Give the extent of all uninfected red blood cells.
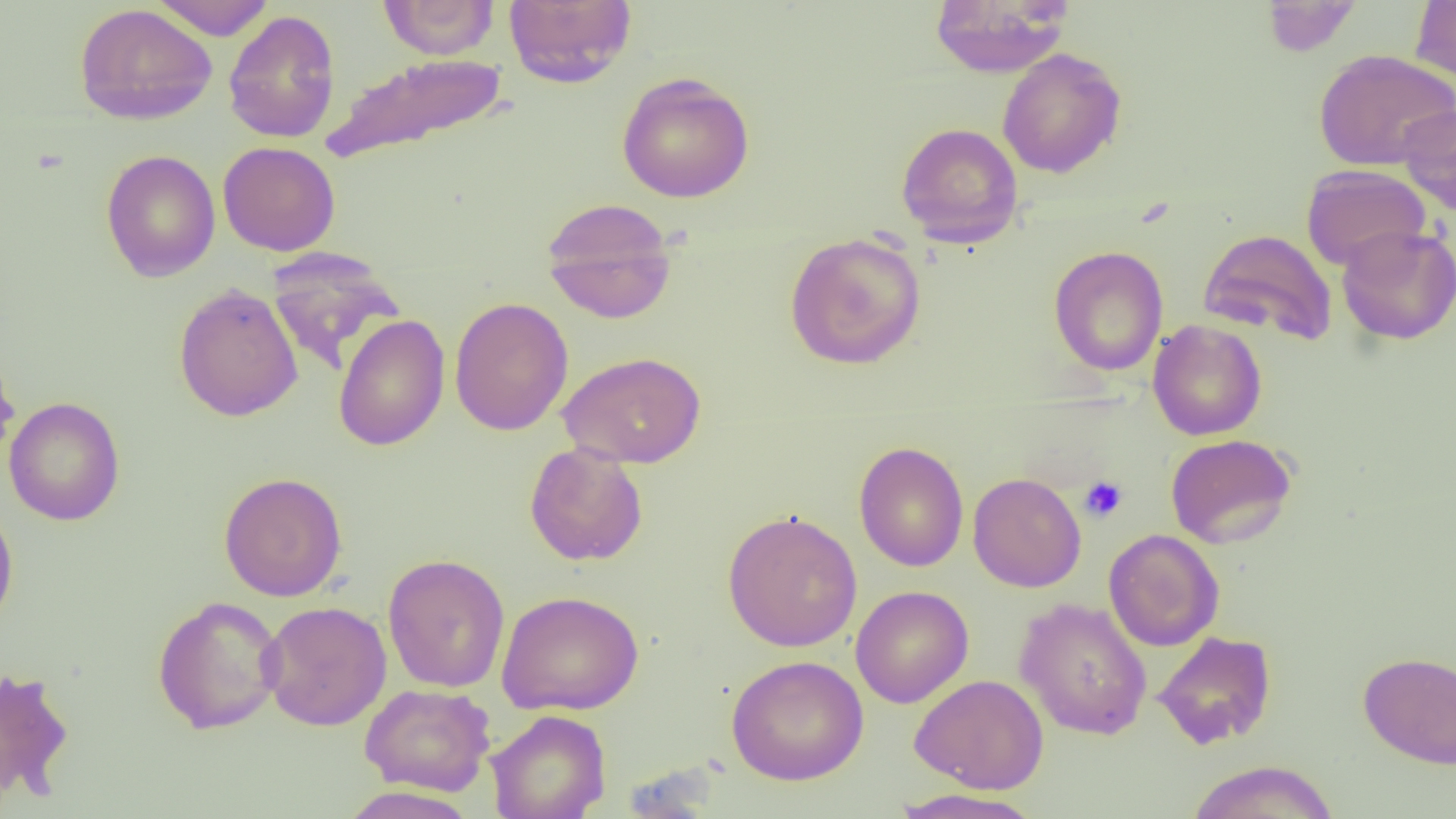
Approximate bounding boxes as [x1, y1, x2, y2] in pixels.
Uninfected red blood cells: [149, 0, 275, 41], [378, 0, 500, 60], [1261, 0, 1363, 57], [503, 1, 637, 87], [928, 1, 1071, 77], [1410, 1, 1456, 82], [75, 3, 217, 125], [223, 9, 341, 143], [997, 48, 1126, 178], [1313, 49, 1456, 171], [323, 52, 510, 163], [616, 71, 755, 203], [1398, 105, 1456, 216], [896, 122, 1024, 247], [217, 141, 340, 256], [100, 149, 221, 282], [1301, 164, 1431, 271], [541, 198, 678, 324], [1336, 225, 1456, 345], [1198, 229, 1339, 345], [784, 231, 927, 370], [1049, 245, 1168, 376], [266, 247, 405, 375], [173, 283, 304, 422], [448, 297, 574, 436], [333, 314, 450, 451], [1148, 320, 1267, 441], [0, 345, 21, 469], [558, 350, 706, 469], [4, 396, 125, 526], [1165, 434, 1298, 550], [854, 441, 969, 572], [524, 443, 648, 566], [218, 471, 348, 602], [968, 472, 1086, 593], [0, 498, 19, 635], [722, 509, 863, 652], [1103, 529, 1224, 652], [383, 553, 510, 693], [850, 585, 973, 709], [496, 590, 644, 715], [152, 595, 286, 735], [1014, 597, 1153, 740], [260, 601, 392, 731], [1152, 630, 1277, 750], [1358, 651, 1456, 770], [726, 655, 868, 785], [0, 665, 74, 805], [910, 673, 1049, 794], [359, 683, 496, 796], [486, 710, 612, 819], [1185, 760, 1341, 819], [337, 786, 479, 819], [890, 787, 1046, 819].

{
  "slide_level_diagnosis": "negative for blood parasites",
  "image_size": "1456×819 pixels",
  "platelet_locations": "approximate bounding boxes as [x1, y1, x2, y2] in pixels: [1079, 476, 1128, 523]",
  "field_of_view": "single",
  "preparation": "thin blood smear",
  "magnification": "1000x",
  "modality": "light microscopy"
}